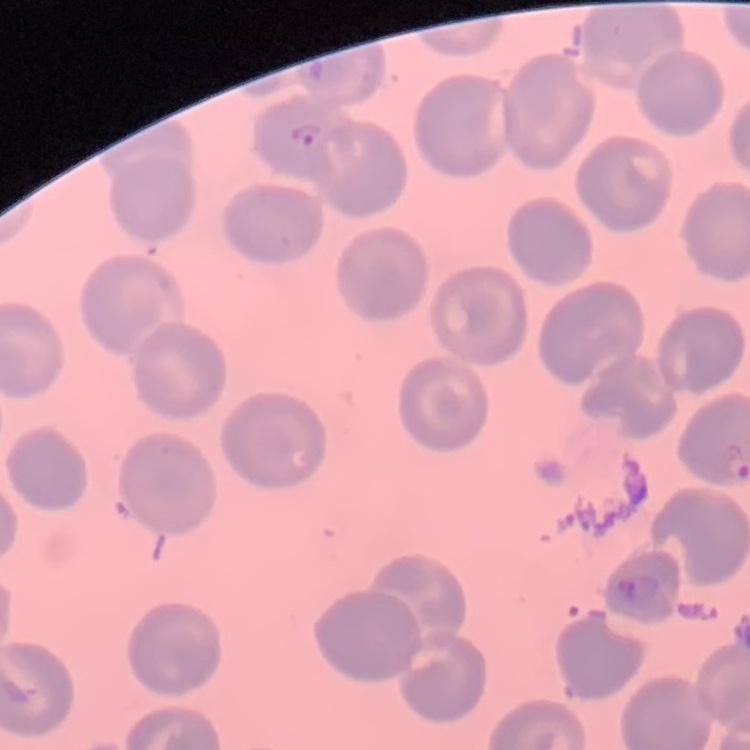

erythrocyte_morphology: no rouleaux formation
image_type: one tile cut from a larger photomicrograph
preparation: thin peripheral smear
stain: Field's or Giemsa